Identify the parasite.
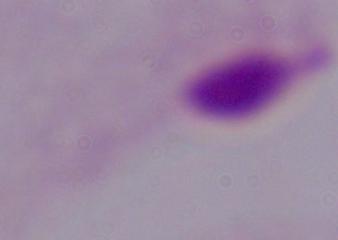
A trichomonad.

modality: micrograph
magnification: 1000x